Comment on the morphology of the red blood cells.
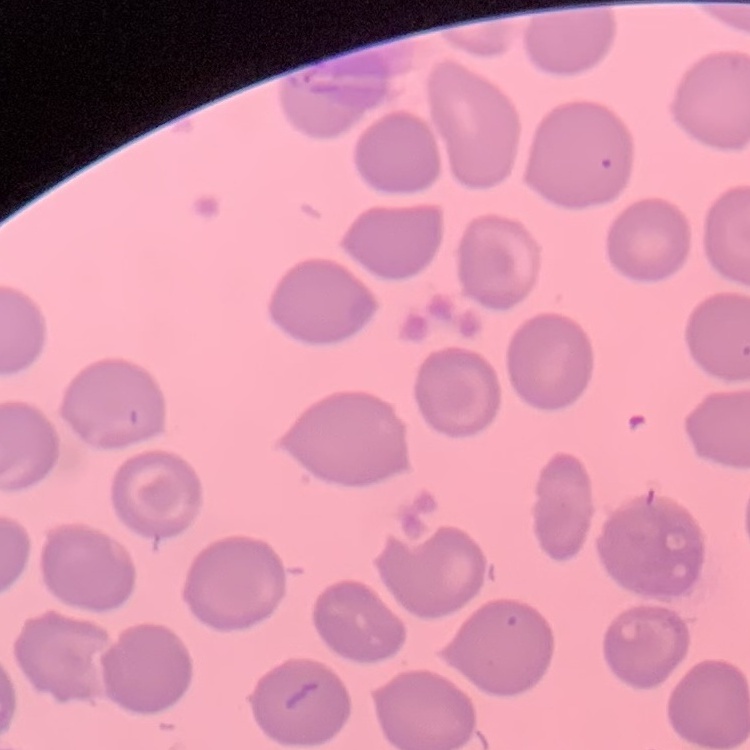
No rouleaux formation.

Thin blood film. Field's or Giemsa stain. Square crop of a larger photomicrograph.